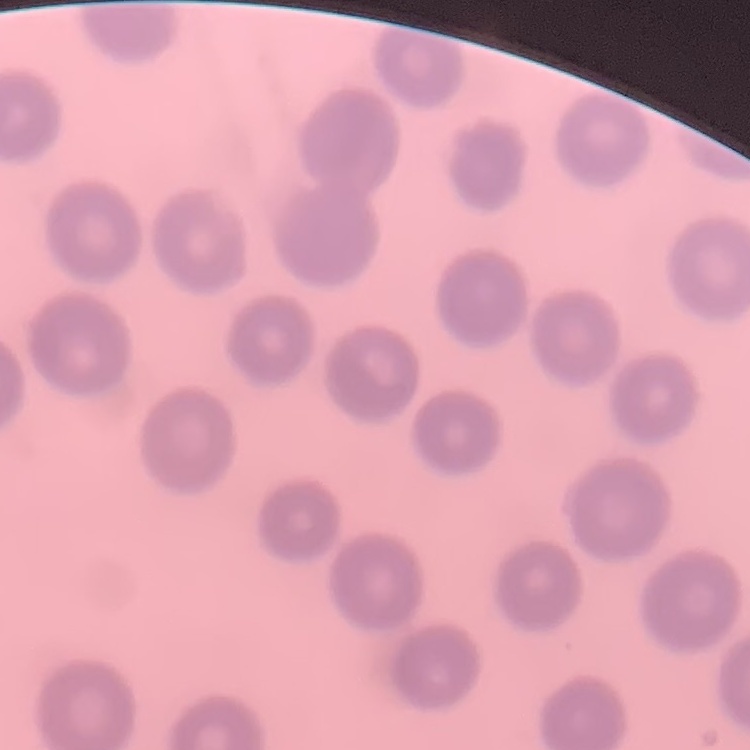
Summary:
  - Erythrocyte morphology: no rouleaux formation
  - Preparation: thin peripheral smear
  - Image type: one tile cut from a larger photomicrograph
  - Stain: Field's or Giemsa